Assess for malaria.
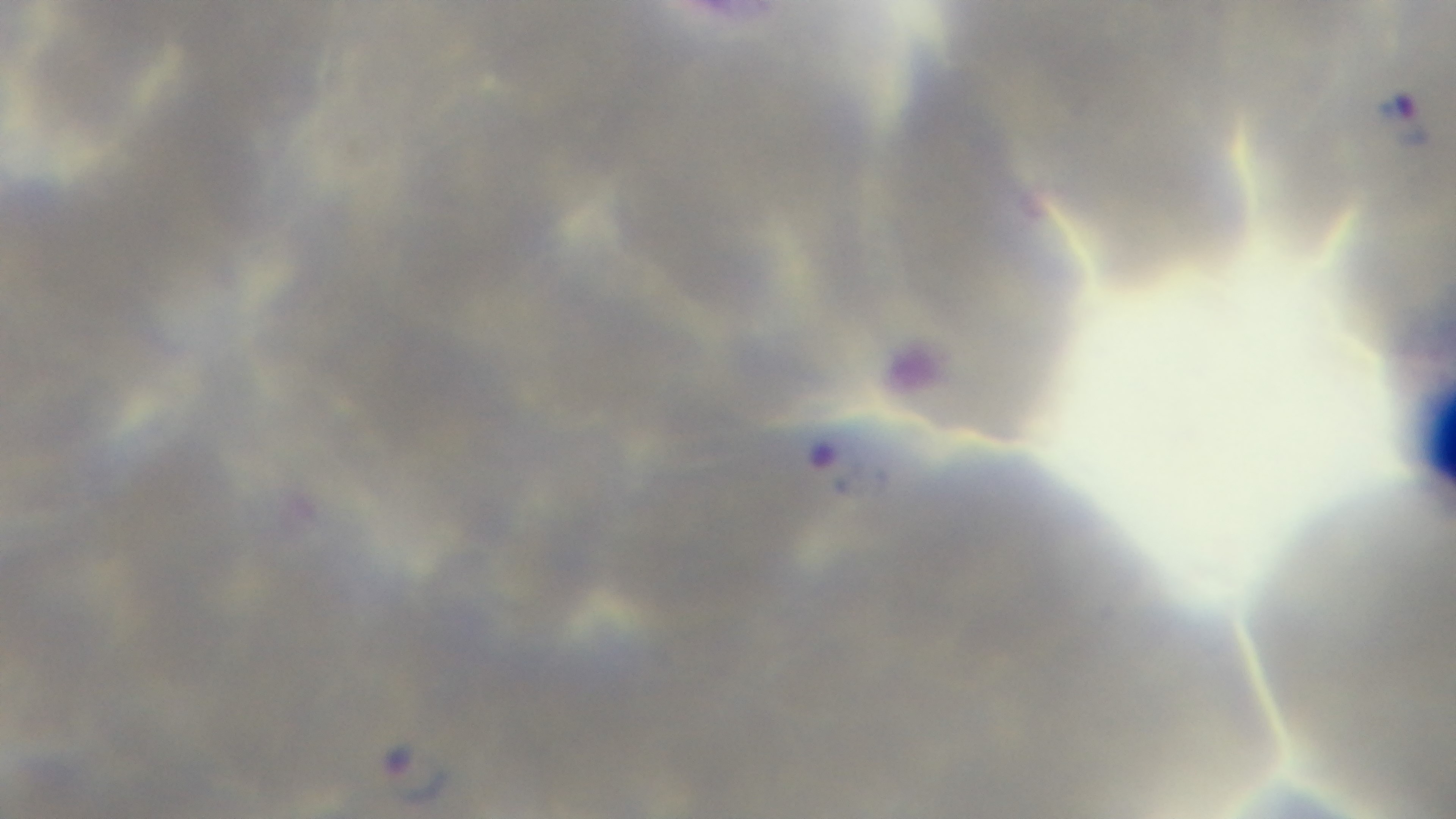
It is infected.

Photomicrograph. 100x oil-immersion objective. Giemsa stain. Preparation: thin. Single field of view. Mounted 4K digital camera.